Describe the morphology of the erythrocytes.
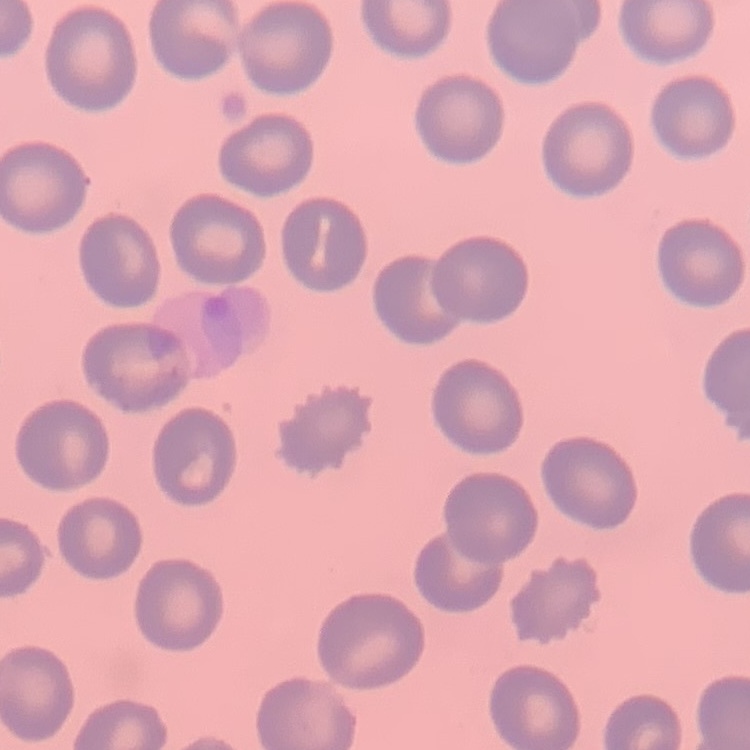

No rouleaux formation.

One tile cut from a larger photomicrograph. Thin peripheral smear. Stained with either Field's or Giemsa.